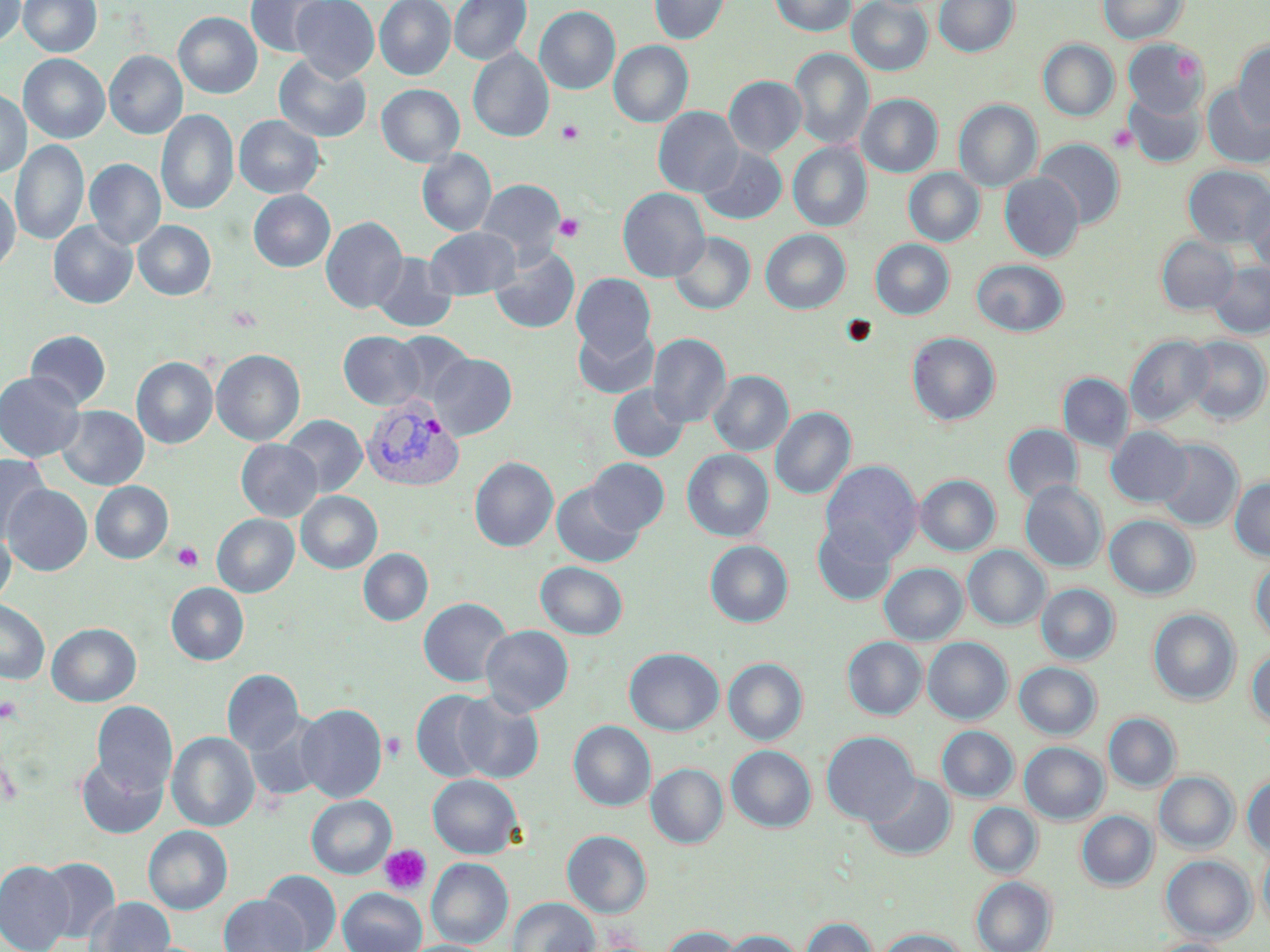

Summary:
  - Coordinate format: approximate bounding boxes as [x1, y1, x2, y2] in pixels
  - Platelet locations: [556, 119, 584, 145], [1108, 124, 1137, 153], [554, 213, 585, 242], [226, 305, 264, 332], [838, 314, 878, 348], [171, 541, 204, 572], [0, 696, 23, 723], [382, 731, 406, 763], [379, 844, 431, 895]
  - Plasmodium vivax-infected red blood cell locations: [361, 393, 463, 491]
  - Uninfected red blood cell locations: [0, 0, 25, 48], [18, 0, 101, 58], [246, 0, 336, 58], [291, 0, 379, 83], [375, 0, 455, 81], [449, 0, 531, 65], [649, 0, 730, 45], [769, 0, 856, 37], [847, 0, 933, 76], [934, 0, 1019, 57], [1097, 0, 1188, 44], [535, 6, 620, 95], [173, 11, 262, 99], [1038, 39, 1119, 121], [1123, 39, 1208, 117], [609, 40, 693, 129], [1234, 41, 1270, 130], [468, 48, 554, 143], [789, 48, 874, 151], [105, 51, 187, 140], [19, 54, 110, 144], [274, 54, 371, 143], [724, 76, 806, 158], [377, 84, 464, 167], [1202, 84, 1270, 168], [1124, 89, 1206, 168], [0, 90, 31, 179], [857, 94, 942, 177], [954, 99, 1042, 193], [653, 107, 743, 198], [156, 109, 239, 216], [234, 115, 324, 199], [11, 139, 89, 247], [1034, 139, 1124, 229], [788, 142, 872, 232], [697, 146, 787, 225], [417, 148, 496, 237], [84, 158, 166, 250], [1183, 165, 1270, 249], [903, 168, 985, 247], [1000, 172, 1084, 261], [476, 180, 565, 262], [0, 184, 21, 274], [617, 188, 709, 282], [248, 189, 335, 272], [1246, 192, 1270, 282], [321, 215, 407, 314], [133, 220, 216, 301], [48, 221, 137, 309], [425, 227, 521, 300], [761, 229, 851, 314], [669, 232, 755, 315], [1156, 235, 1239, 315], [870, 239, 954, 320], [489, 245, 580, 334], [369, 252, 457, 333], [971, 259, 1069, 337], [1209, 263, 1270, 339], [571, 273, 656, 360], [573, 323, 659, 400], [25, 330, 111, 409], [338, 331, 425, 410], [386, 331, 475, 409], [906, 332, 1000, 426], [648, 333, 731, 429], [1125, 334, 1214, 426], [1184, 336, 1270, 424], [211, 349, 305, 447], [428, 353, 517, 440], [131, 356, 218, 449], [708, 370, 793, 456], [0, 371, 85, 462], [1058, 372, 1134, 454], [608, 384, 690, 462], [56, 405, 149, 490], [771, 406, 856, 501], [282, 415, 367, 497], [1002, 424, 1083, 503], [1106, 426, 1193, 506], [236, 439, 322, 521], [1155, 440, 1243, 532], [682, 449, 774, 542], [0, 454, 51, 545], [470, 456, 558, 552], [587, 458, 669, 535], [821, 460, 923, 564], [915, 474, 1000, 556], [1229, 477, 1270, 561], [1020, 480, 1108, 573], [90, 481, 173, 564], [551, 482, 644, 568], [2, 484, 92, 576], [296, 491, 382, 574], [212, 513, 299, 597], [1104, 515, 1200, 600], [813, 522, 895, 605], [0, 525, 15, 608], [705, 540, 793, 628], [963, 545, 1050, 631], [359, 548, 433, 626], [1249, 558, 1270, 648], [535, 562, 628, 640], [879, 563, 968, 646], [166, 583, 249, 665], [1028, 583, 1110, 739], [1036, 583, 1120, 665], [418, 597, 512, 688], [0, 599, 50, 684], [1148, 609, 1240, 706], [47, 623, 141, 707], [481, 625, 574, 716], [842, 637, 927, 720], [923, 637, 1012, 724], [624, 647, 724, 736], [1246, 647, 1270, 730], [723, 658, 807, 746], [1014, 662, 1102, 740], [222, 669, 304, 756], [411, 690, 496, 783], [452, 691, 544, 784], [92, 701, 178, 796], [296, 703, 387, 802], [1104, 712, 1181, 792], [246, 714, 329, 803], [568, 720, 656, 812], [937, 726, 1019, 803], [167, 731, 260, 832], [821, 731, 919, 826], [1019, 742, 1108, 824], [726, 745, 816, 832], [76, 755, 167, 838], [646, 763, 728, 848], [1154, 771, 1239, 854], [863, 773, 956, 861], [1242, 773, 1270, 857], [427, 774, 522, 859], [307, 795, 396, 879], [967, 802, 1042, 878], [1076, 811, 1158, 891], [143, 825, 233, 915], [562, 830, 652, 919], [1258, 844, 1270, 937], [1160, 855, 1256, 942], [36, 857, 120, 943], [426, 858, 513, 949], [0, 860, 75, 952], [260, 870, 341, 952], [971, 876, 1057, 951], [338, 888, 427, 952], [219, 895, 309, 952], [85, 897, 175, 952], [509, 897, 600, 952], [801, 917, 878, 952], [661, 926, 742, 952], [874, 928, 971, 952], [718, 930, 807, 952], [1145, 938, 1235, 952], [401, 940, 494, 952]
  - Slide-level diagnosis: Plasmodium vivax
  - Modality: optical microscopy
  - Preparation: thin blood smear
  - Image size: 1270×952 pixels
  - Field of view: one of a larger specimen
  - Magnification: 1000x
  - Stain: May-Grünwald-Giemsa